Assess this cell for malaria.
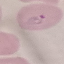
It is parasitized.

Photographed with a smartphone camera at the microscope eyepiece. Thin blood smear. Giemsa stain. Automatically extracted cell patch, resized to 64 × 64 pixels.